Assess the morphology of the red blood cells.
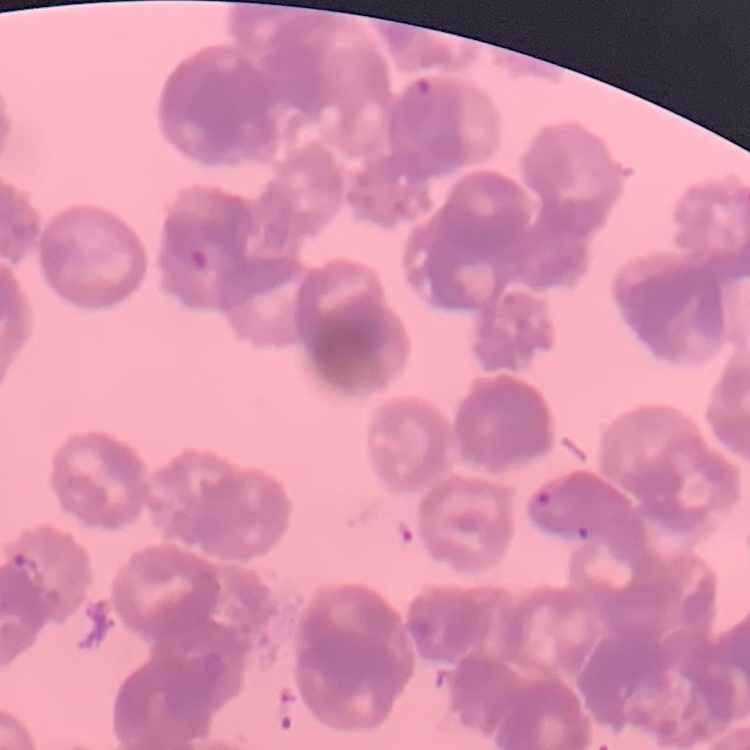

They show rouleaux formation.

Field's or Giemsa stain. Square crop of a larger photomicrograph. Thin peripheral smear.